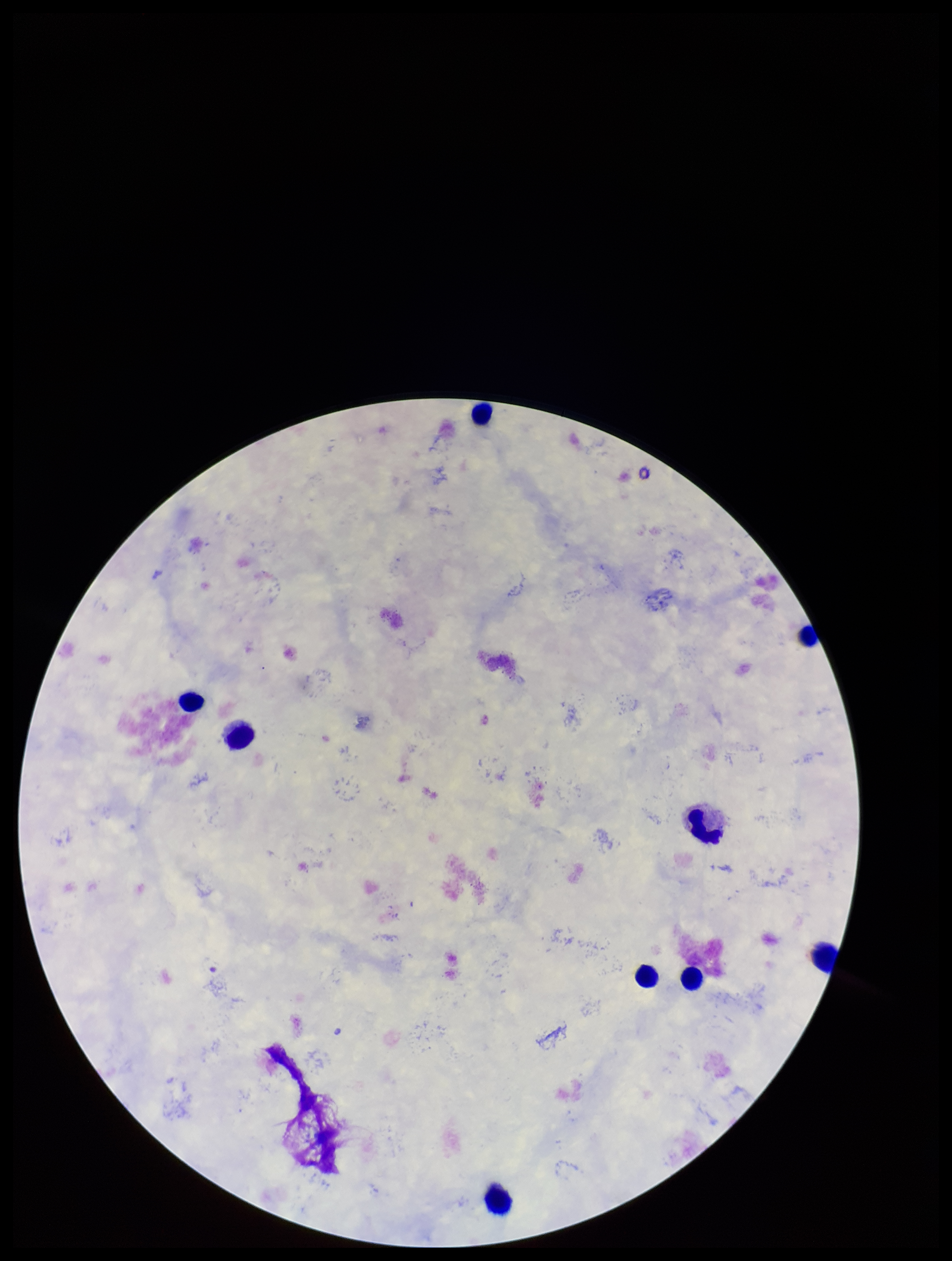
leukocyte count = 9
stain = Giemsa
parasite count = 0
species reported for this patient = Plasmodium falciparum
Plasmodium parasites = none seen
image size = 952×1261 pixels
capture = smartphone photograph through the microscope eyepiece
patient malaria status = positive
preparation = thick blood smear
field of view = one from this slide